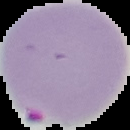
Summary:
  - Result: malaria parasites identified
  - Image type: segmented cell region on a black background
  - Preparation: thin blood smear
  - Image size: 130×130 pixels